Locate every malaria parasite.
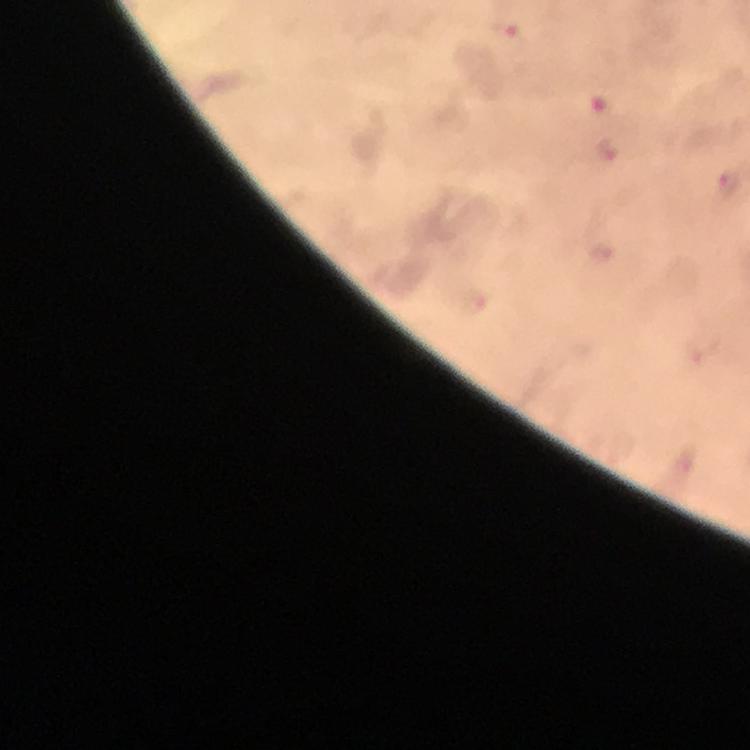

Approximate object centers, in pixels from the top-left corner.
Malaria parasites: (x=517, y=35), (x=728, y=184).

Summary:
  - Capture: smartphone photograph through a microscope
  - Cropped from: one field of view
  - Stain: Giemsa
  - Context: from a malaria diagnostic workup
  - Image size: 750×750 pixels
  - Magnification: 100x
  - Immersion oil: applied
  - Preparation: thick smear